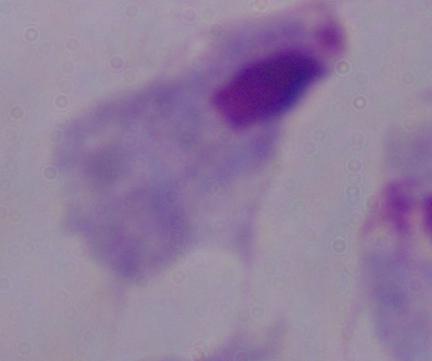
Summary:
  - Magnification: 1000x
  - Modality: micrograph
  - Identification: trichomonad